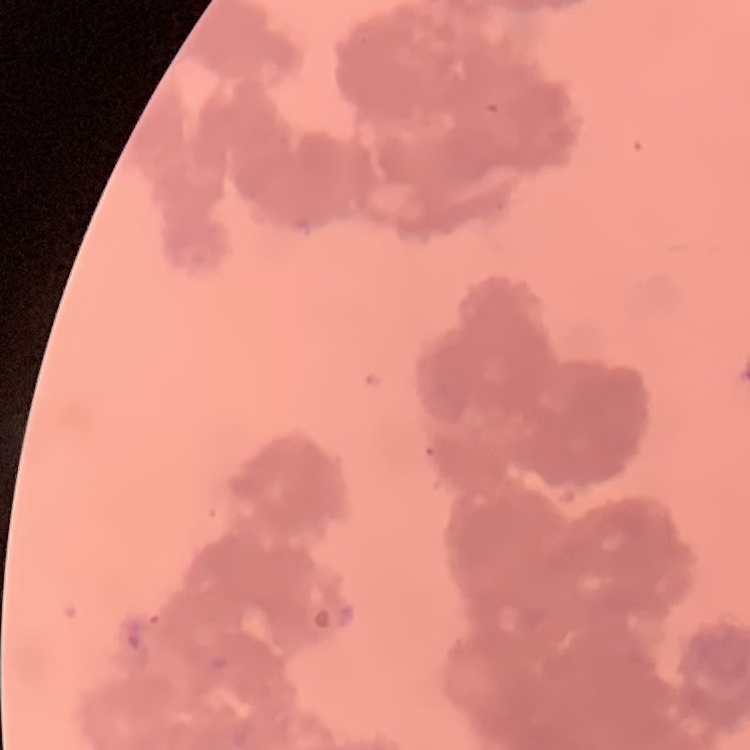

Summary:
  - Red blood cell morphology: rouleaux formation
  - Preparation: thin peripheral smear
  - Stain: Field's or Giemsa
  - Image type: one tile cut from a larger photomicrograph